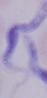

Summary:
  - Magnification: 1000x
  - Modality: photomicrograph
  - Identification: trypanosome